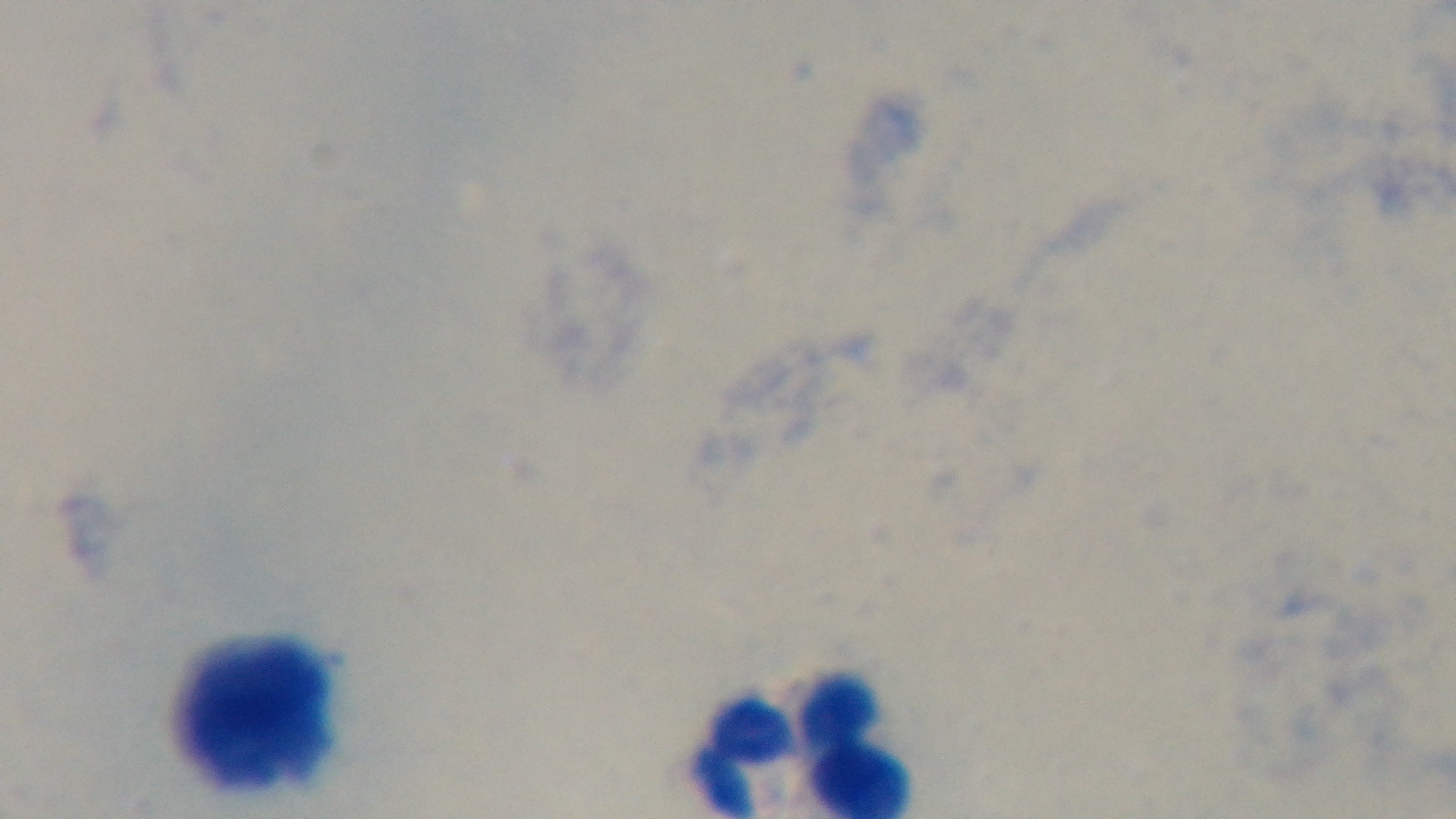
Summary:
  - Stain: Giemsa
  - Field of view: one from the slide
  - Objective: 100x oil immersion
  - Malaria status: negative
  - Capture: mounted 4K digital camera
  - Modality: light microscopy
  - Preparation: thick